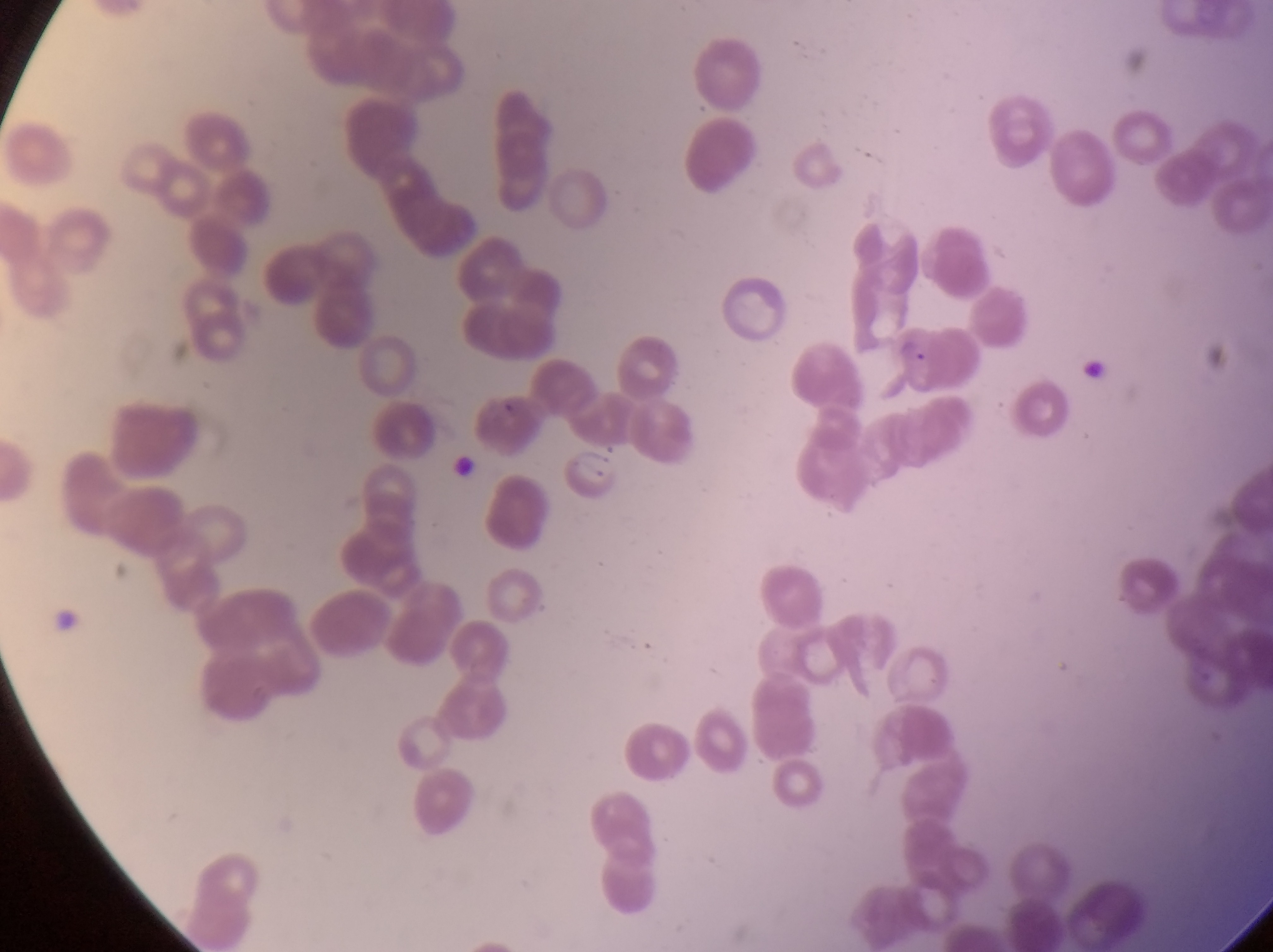
image size = 1273×952 pixels
country = Uganda
parasitised red blood cell locations = approximate bounding boxes as {left, top, right, bottom} in pixels: {888, 317, 963, 395}, {567, 441, 624, 501}
capture = smartphone photograph through the eyepiece of an Olympus CX-23 microscope
magnification = 1000x
preparation = thin blood smear
artifact (platelet-like body, stain precipitate, or debris) locations = approximate bounding boxes as {left, top, right, bottom} in pixels: {1071, 355, 1108, 383}, {445, 447, 475, 492}
field of view = single